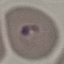

result = malaria parasites identified
image type = cell patch, automatically extracted from a larger field of view and resized to 64 × 64 pixels
capture = smartphone through the microscope eyepiece
stain = Giemsa
preparation = thin blood film